Comment on the morphology of the erythrocytes.
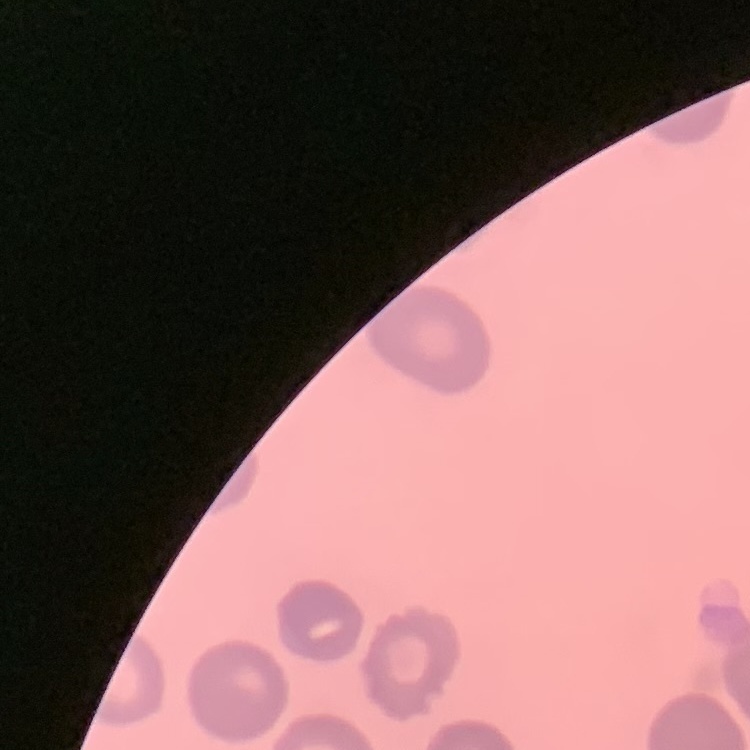
They show no rouleaux formation.

Summary:
  - Stain: Field's or Giemsa
  - Preparation: thin peripheral smear
  - Image type: square crop of a larger photomicrograph